Describe the morphology of the erythrocytes.
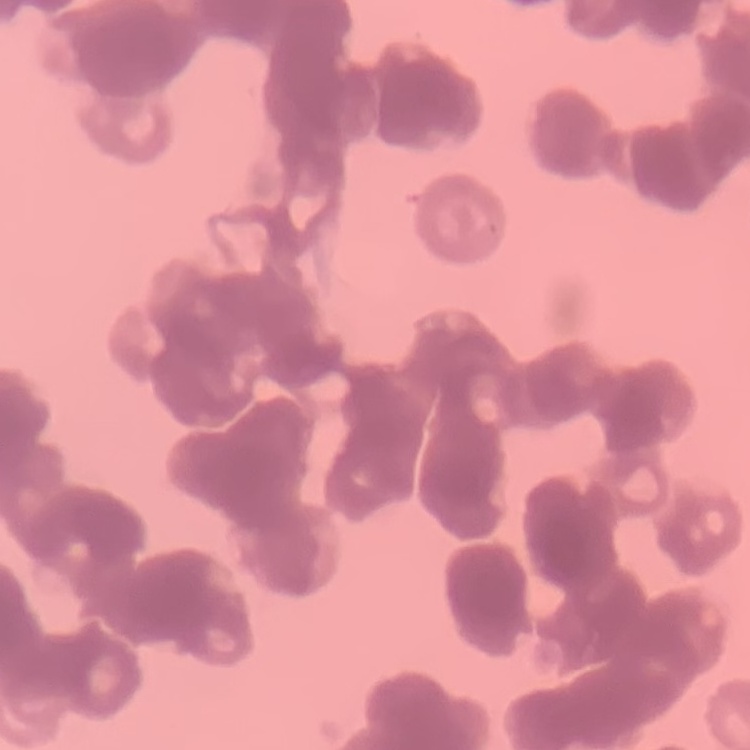
They show rouleaux formation.

Summary:
  - Image type: square crop of a larger photomicrograph
  - Preparation: thin peripheral smear
  - Stain: Field's or Giemsa